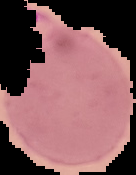

Image is 136×175 pixels. Result: Plasmodium parasites detected. The area outside the segmented cell region is set to black. From a thin blood smear.